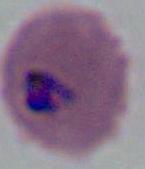

A Plasmodium parasite is seen. Captured at either 400x or 1000x magnification. Photomicrograph.